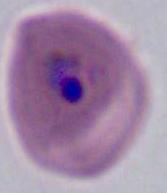
{
  "modality": "micrograph",
  "magnification": "400x or 1000x",
  "identification": "Plasmodium"
}